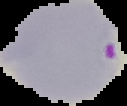

Result: malaria parasites identified. Image is 127×106 pixels. From a thin blood smear. The area outside the segmented cell region is set to black.